Comment on the morphology of the erythrocytes.
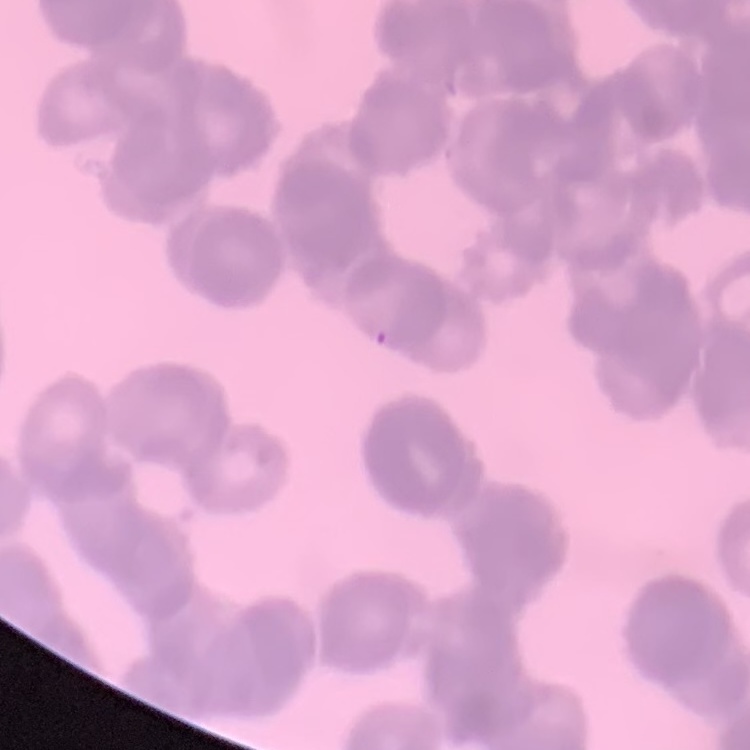

They show rouleaux formation.

One tile cut from a larger photomicrograph. Field's or Giemsa stain. Thin peripheral smear.